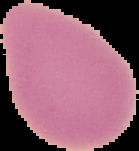

Image is 139×151 pixels. From a thin blood film. Cell region segmented out of the field of view; the surrounding area is masked to black. Result: no Plasmodium parasites detected.